Give the extent of all Plasmodium vivax-infected red blood cells.
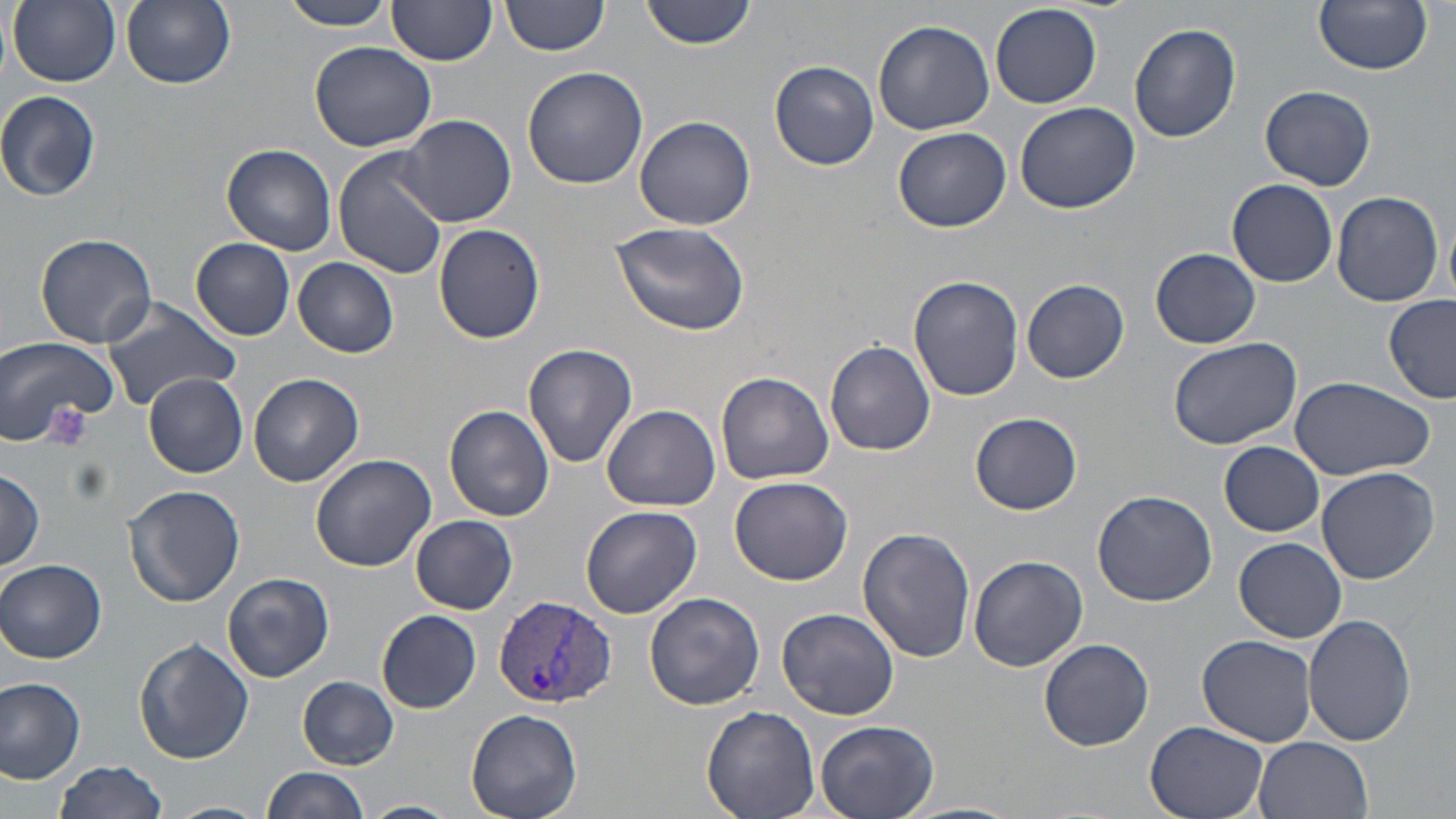
Approximate bounding boxes as (x1, y1, x2, y2) in pixels.
Plasmodium vivax-infected red blood cells: (493, 594, 616, 711).

Summary:
  - Uninfected red blood cell locations: (8, 0, 121, 88), (121, 0, 237, 90), (280, 0, 397, 31), (501, 0, 613, 57), (641, 0, 758, 49), (1315, 0, 1433, 74), (389, 3, 496, 66), (990, 5, 1102, 108), (873, 18, 996, 135), (1130, 24, 1242, 144), (310, 39, 440, 151), (770, 61, 879, 170), (522, 66, 649, 190), (1261, 85, 1376, 191), (0, 90, 102, 202), (1015, 102, 1140, 214), (399, 113, 515, 226), (634, 115, 756, 231), (893, 127, 1011, 233), (223, 143, 338, 254), (334, 148, 449, 278), (1227, 179, 1338, 288), (1331, 191, 1444, 309), (611, 220, 751, 335), (433, 224, 545, 344), (36, 233, 158, 349), (191, 237, 296, 341), (1151, 247, 1261, 349), (293, 257, 399, 358), (908, 275, 1024, 400), (1022, 280, 1129, 383), (1384, 294, 1456, 402), (101, 300, 243, 414), (0, 335, 120, 447), (1166, 336, 1301, 450), (825, 341, 935, 455), (522, 343, 638, 469), (142, 372, 248, 476), (716, 372, 833, 486), (249, 373, 364, 486), (1289, 375, 1433, 481), (602, 404, 720, 511), (445, 405, 555, 521), (970, 412, 1083, 515), (1220, 441, 1325, 536), (309, 452, 435, 571), (1315, 465, 1440, 585), (0, 469, 45, 571), (730, 475, 853, 585), (124, 485, 245, 609), (1093, 489, 1217, 606), (581, 504, 702, 619), (411, 515, 517, 614), (857, 527, 976, 662), (1234, 537, 1347, 643), (968, 555, 1088, 674), (0, 559, 107, 664), (224, 573, 335, 683), (644, 591, 766, 710), (774, 606, 901, 720), (377, 611, 481, 713), (1300, 614, 1419, 747), (1198, 634, 1318, 747), (134, 638, 255, 765), (1038, 638, 1154, 751), (0, 676, 88, 782), (298, 677, 399, 768), (702, 705, 819, 819), (464, 709, 582, 819), (1144, 719, 1272, 819), (814, 720, 938, 819), (1253, 737, 1373, 819), (54, 760, 170, 819), (261, 766, 368, 819), (359, 799, 462, 819), (162, 801, 267, 819)
  - Slide-level diagnosis: Plasmodium vivax
  - Modality: light microscopy
  - Magnification: 1000x
  - Stain: May-Grünwald-Giemsa
  - Image size: 1456×819 pixels
  - Preparation: thin blood film
  - Field of view: one of a larger specimen